Report the malaria status of this cell.
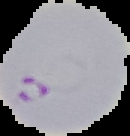
It is parasitized.

image size = 130×136 pixels
image type = segmented cell region on a black background
preparation = thin blood smear